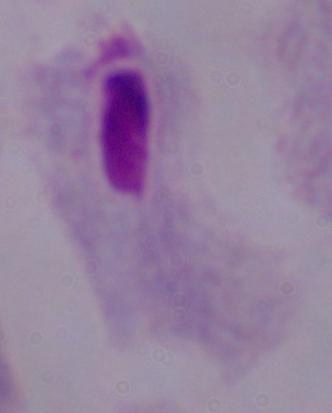
Summary:
  - Modality: photomicrograph
  - Magnification: 1000x
  - Identification: trichomonad